Classify this cell by malaria status.
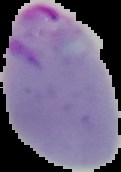

It is parasitized.

Cell region segmented out of the field of view; the surrounding area is masked to black. From a thin blood film. Image is 121×172 pixels.